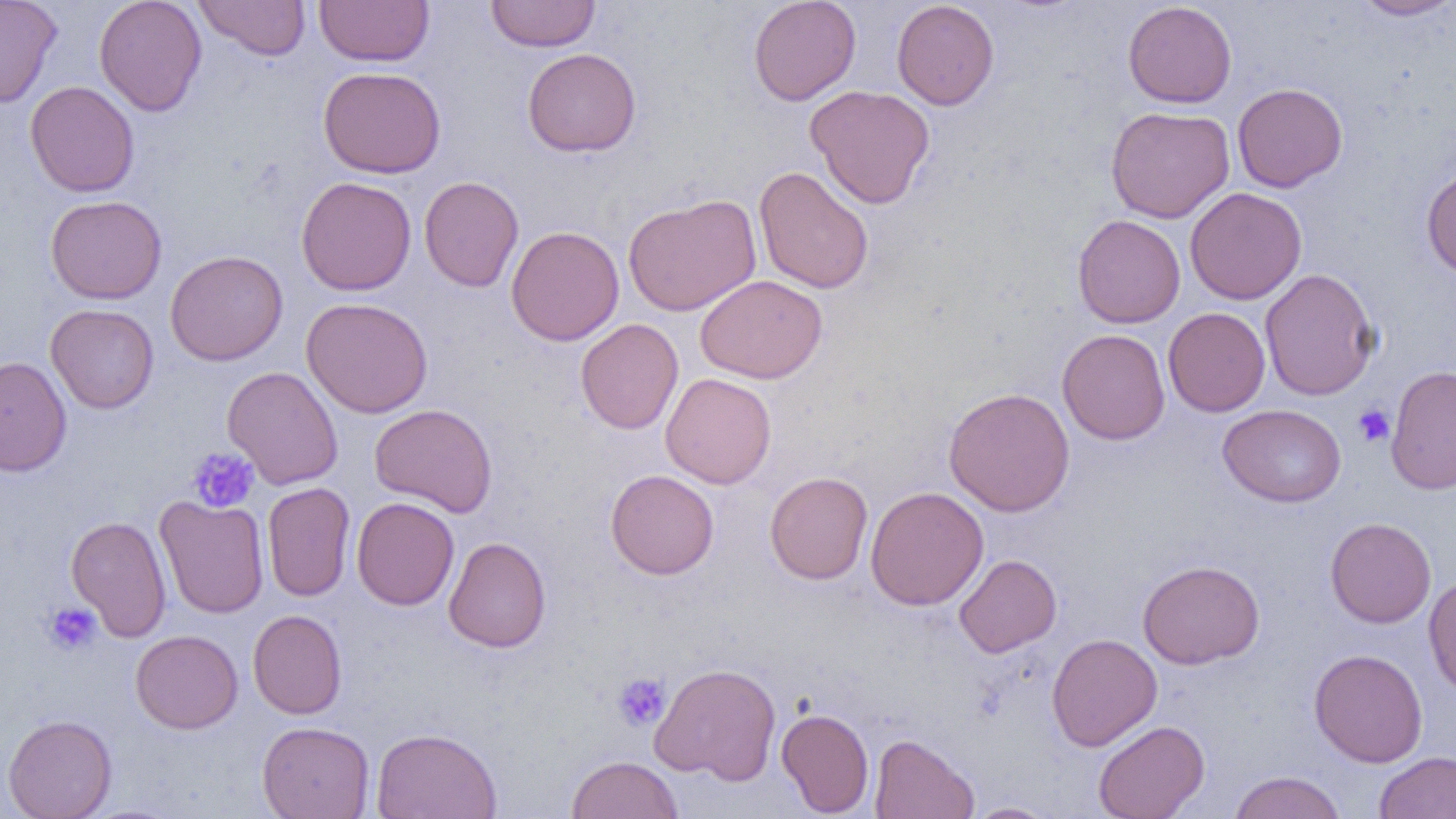
Summary:
  - Coordinate format: approximate bounding boxes as (x1,y1)-(x2,y2) corner pairs in pixels
  - Platelet locations: (1353,404)-(1395,447), (187,447)-(259,513), (43,601)-(102,655), (613,671)-(671,731)
  - Uninfected red blood cell locations: (0,0)-(62,108), (94,0)-(207,116), (193,0)-(311,61), (314,0)-(434,67), (486,0)-(601,52), (748,0)-(862,106), (891,0)-(1000,110), (1350,0)-(1456,21), (1122,1)-(1237,108), (522,48)-(642,157), (318,66)-(446,178), (25,80)-(139,197), (1232,82)-(1347,192), (805,84)-(936,209), (1105,105)-(1235,224), (753,166)-(874,294), (1421,166)-(1456,280), (296,176)-(417,296), (419,176)-(524,292), (1185,187)-(1307,305), (622,194)-(761,316), (45,195)-(167,304), (1072,213)-(1186,328), (505,225)-(624,346), (165,250)-(288,366), (1260,268)-(1380,402), (695,274)-(828,384), (301,297)-(433,418), (45,303)-(159,413), (1163,307)-(1271,417), (575,318)-(684,435), (1057,328)-(1170,445), (0,355)-(72,477), (1386,363)-(1456,496), (222,366)-(343,489), (660,373)-(776,489), (943,387)-(1075,516), (369,403)-(498,518), (1218,404)-(1346,507), (605,469)-(720,580), (764,471)-(873,585), (261,482)-(355,601), (865,486)-(989,610), (154,495)-(269,618), (351,497)-(459,610), (65,515)-(172,641), (1325,517)-(1436,628), (443,536)-(551,653), (954,554)-(1061,657), (1137,559)-(1264,669), (1422,574)-(1456,699), (247,610)-(347,719), (130,629)-(243,734), (1046,633)-(1162,751), (1308,648)-(1428,767), (649,662)-(782,783), (776,708)-(874,816), (3,714)-(117,819), (1093,720)-(1209,819), (257,721)-(374,819), (371,727)-(502,818), (870,733)-(979,818), (1373,751)-(1456,818), (566,755)-(684,819), (1227,770)-(1346,819), (963,801)-(1063,819)
  - Slide-level diagnosis: negative for blood parasites
  - Field of view: single
  - Preparation: thin blood film
  - Image size: 1456×819 pixels
  - Modality: optical microscopy
  - Magnification: 1000x